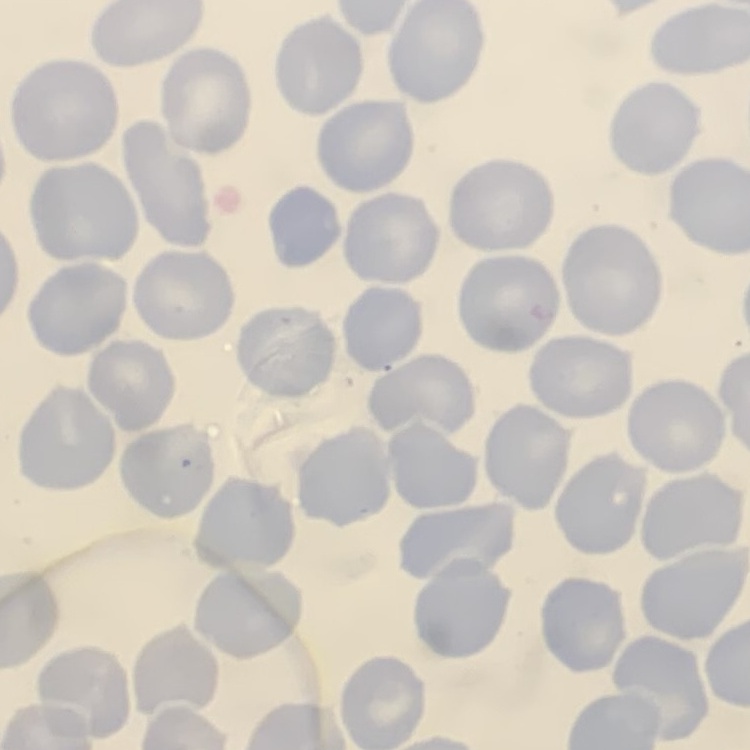
Summary:
  - Erythrocyte morphology: no rouleaux formation
  - Preparation: thin blood film
  - Image type: square crop of a larger photomicrograph
  - Stain: Field's or Giemsa